Assess the morphology of the erythrocytes.
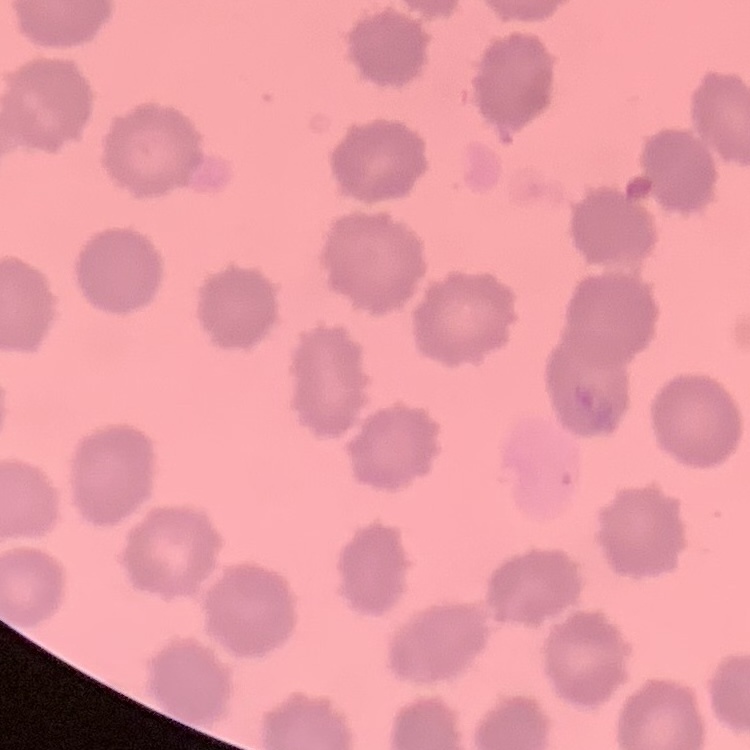

No rouleaux formation.

image type = one tile cut from a larger photomicrograph
preparation = thin peripheral smear
stain = Field's or Giemsa